Describe the morphology of the erythrocytes.
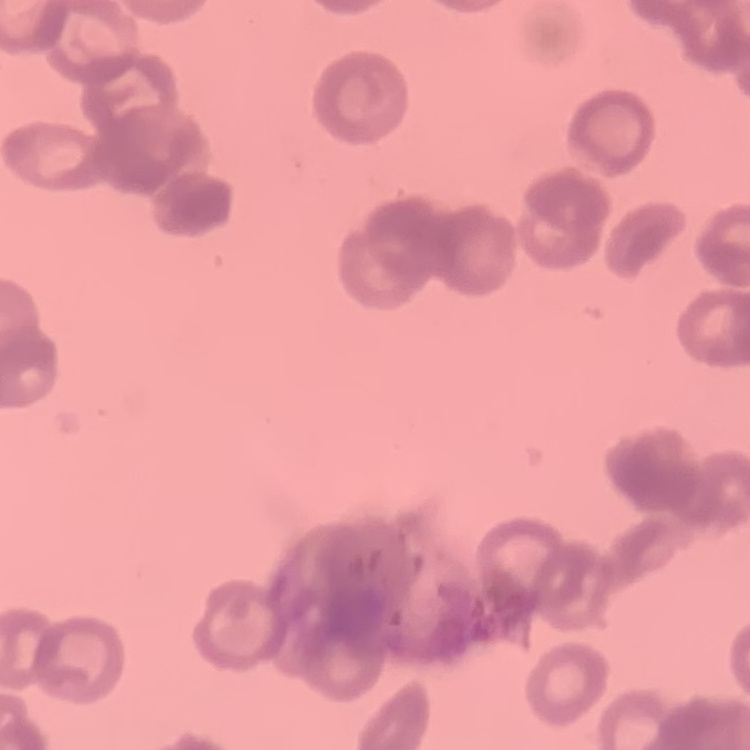
Rouleaux formation.

Stained with either Field's or Giemsa. One tile cut from a larger photomicrograph. Thin blood film.